Locate every uninfected red blood cell.
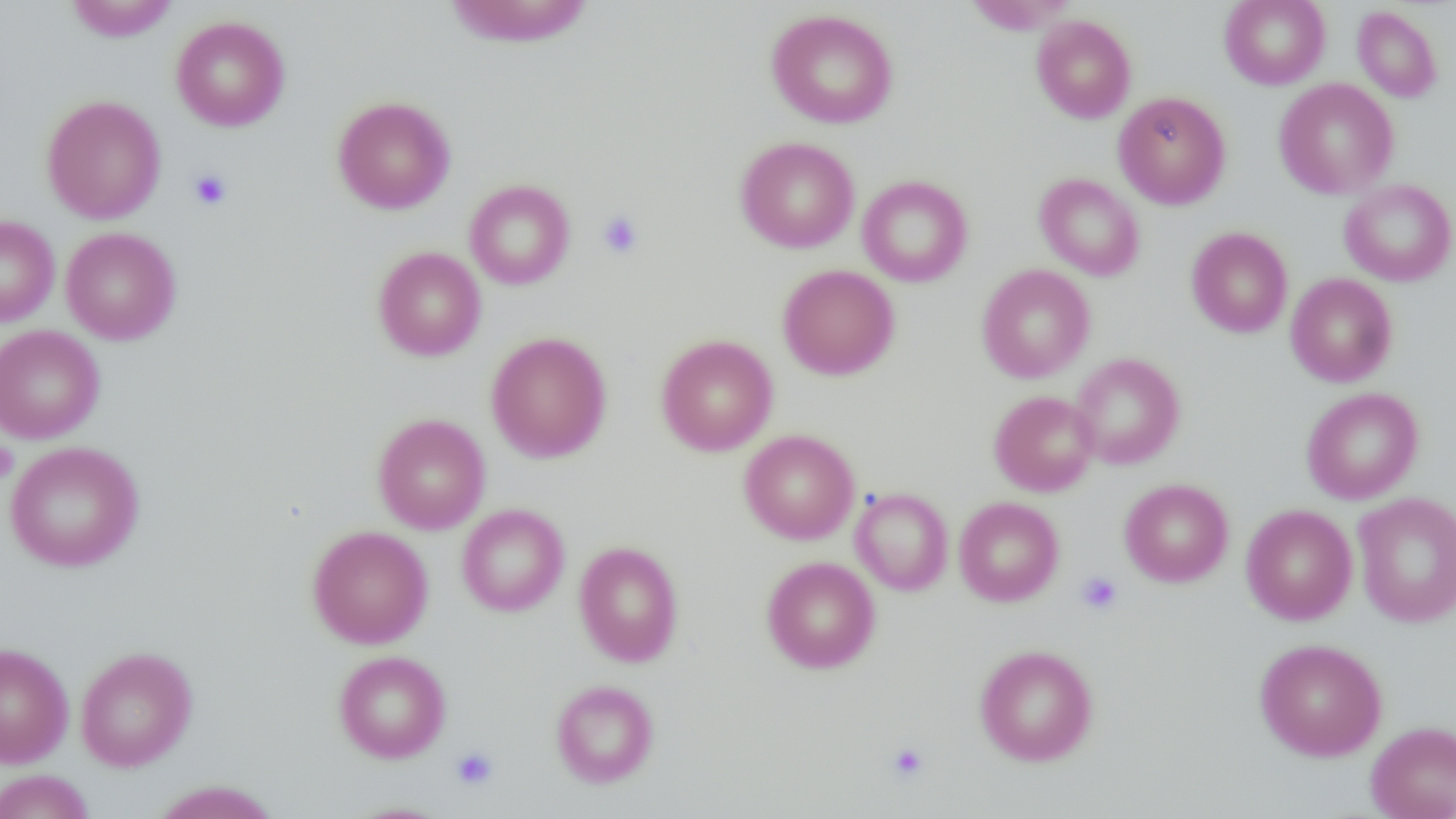
Approximate bounding boxes as [x1, y1, x2, y2] in pixels.
Uninfected red blood cells: [64, 0, 179, 42], [962, 0, 1080, 35], [1220, 0, 1331, 89], [443, 1, 595, 48], [1352, 5, 1443, 103], [766, 9, 899, 129], [170, 15, 290, 132], [1031, 15, 1136, 123], [1274, 78, 1399, 199], [1114, 91, 1231, 209], [41, 95, 166, 224], [332, 96, 456, 214], [735, 136, 859, 253], [1034, 173, 1145, 281], [857, 175, 973, 287], [1339, 179, 1456, 286], [464, 180, 575, 290], [0, 215, 59, 326], [1186, 226, 1293, 338], [61, 227, 181, 345], [373, 246, 486, 361], [777, 264, 900, 380], [976, 264, 1095, 383], [1285, 273, 1398, 387], [0, 324, 104, 444], [486, 332, 612, 463], [656, 334, 778, 456], [1069, 352, 1185, 469], [1301, 387, 1423, 504], [989, 390, 1100, 496], [372, 413, 490, 534], [739, 429, 859, 544], [4, 441, 144, 571], [1120, 478, 1233, 587], [850, 487, 953, 595], [1352, 492, 1456, 627], [954, 496, 1064, 606], [456, 504, 569, 617], [1241, 504, 1358, 625], [307, 525, 433, 649], [574, 541, 684, 667], [762, 556, 880, 673], [1254, 638, 1387, 761], [0, 643, 74, 767], [975, 644, 1098, 766], [75, 646, 197, 771], [333, 650, 451, 762], [551, 680, 659, 788], [1366, 720, 1456, 819], [0, 769, 95, 819], [150, 780, 281, 819], [341, 801, 455, 819].

Summary:
  - Platelet locations: [188, 168, 233, 211], [597, 210, 644, 259], [0, 441, 18, 482], [1077, 571, 1123, 615], [887, 742, 929, 782], [451, 747, 498, 790]
  - Slide-level diagnosis: negative for blood parasites
  - Magnification: 1000x
  - Preparation: thin blood film
  - Modality: optical microscopy
  - Image size: 1456×819 pixels
  - Field of view: one of a larger specimen